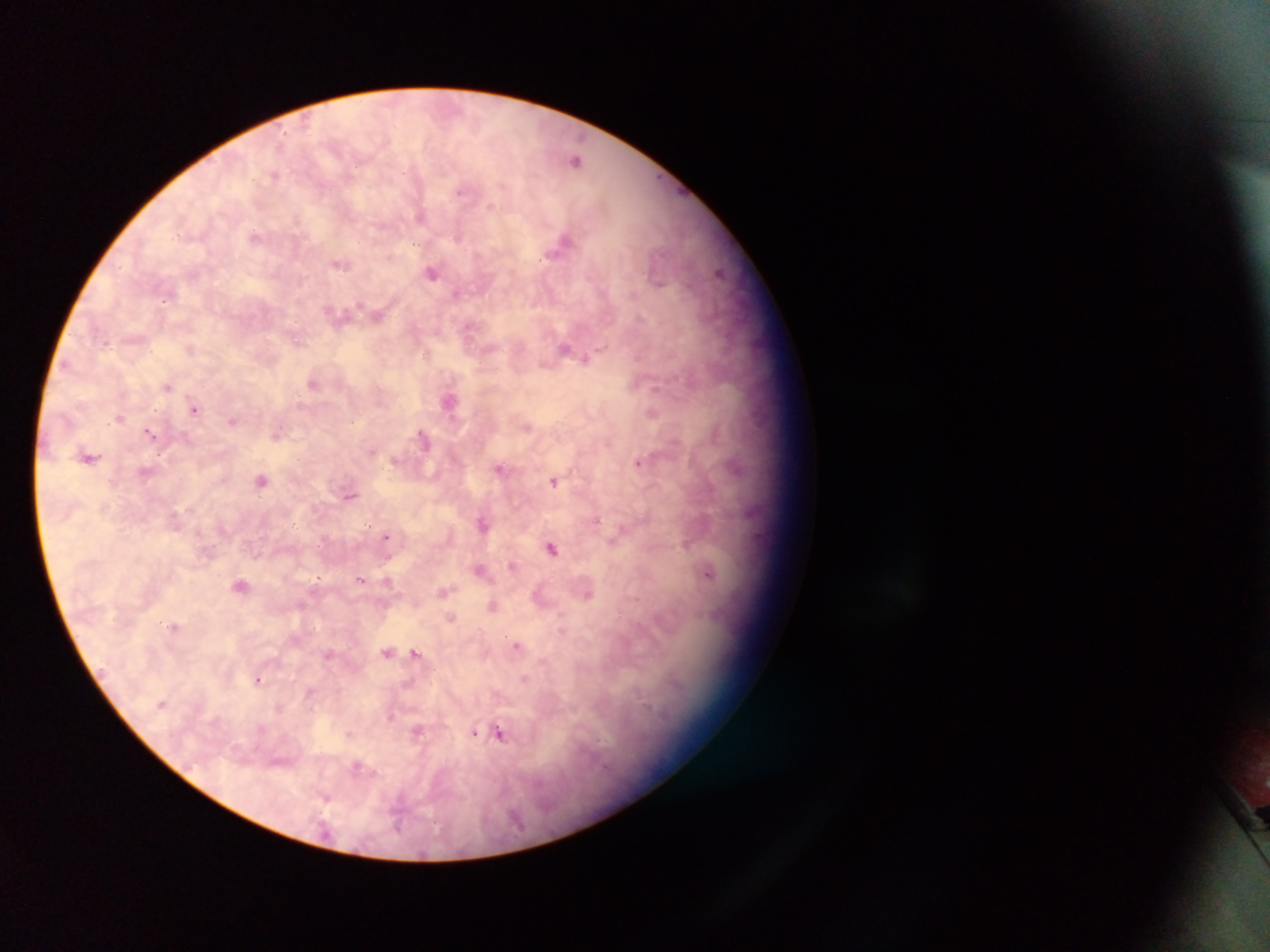
Approximate centers as {x, y} in pixels. Malaria parasite locations: {577, 160}, {275, 174}, {422, 215}, {257, 236}, {565, 242}, {340, 263}, {432, 271}, {721, 272}, {338, 313}, {378, 314}, {566, 348}, {192, 349}, {586, 358}, {313, 382}, {168, 385}, {450, 400}, {195, 407}, {653, 413}, {119, 416}, {234, 420}, {526, 425}, {151, 433}, {277, 434}, {424, 438}, {90, 456}, {395, 460}, {640, 462}, {499, 468}, {147, 472}, {262, 479}, {554, 481}, {350, 494}, {175, 520}, {483, 522}, {386, 536}, {687, 542}, {552, 547}, {513, 565}, {481, 569}, {709, 571}, {361, 580}, {242, 584}, {444, 590}, {587, 590}, {540, 596}, {493, 605}, {451, 618}, {175, 627}, {562, 630}, {517, 646}, {387, 651}, {416, 653}, {329, 654}, {259, 678}, {526, 679}, {418, 730}, {349, 733}, {474, 733}, {480, 733}, {499, 733}, {327, 796}. Single field of view. Sample from Ghana. Thick blood film. Mobile-phone photograph taken through the microscope. Image is 1270×952 pixels.